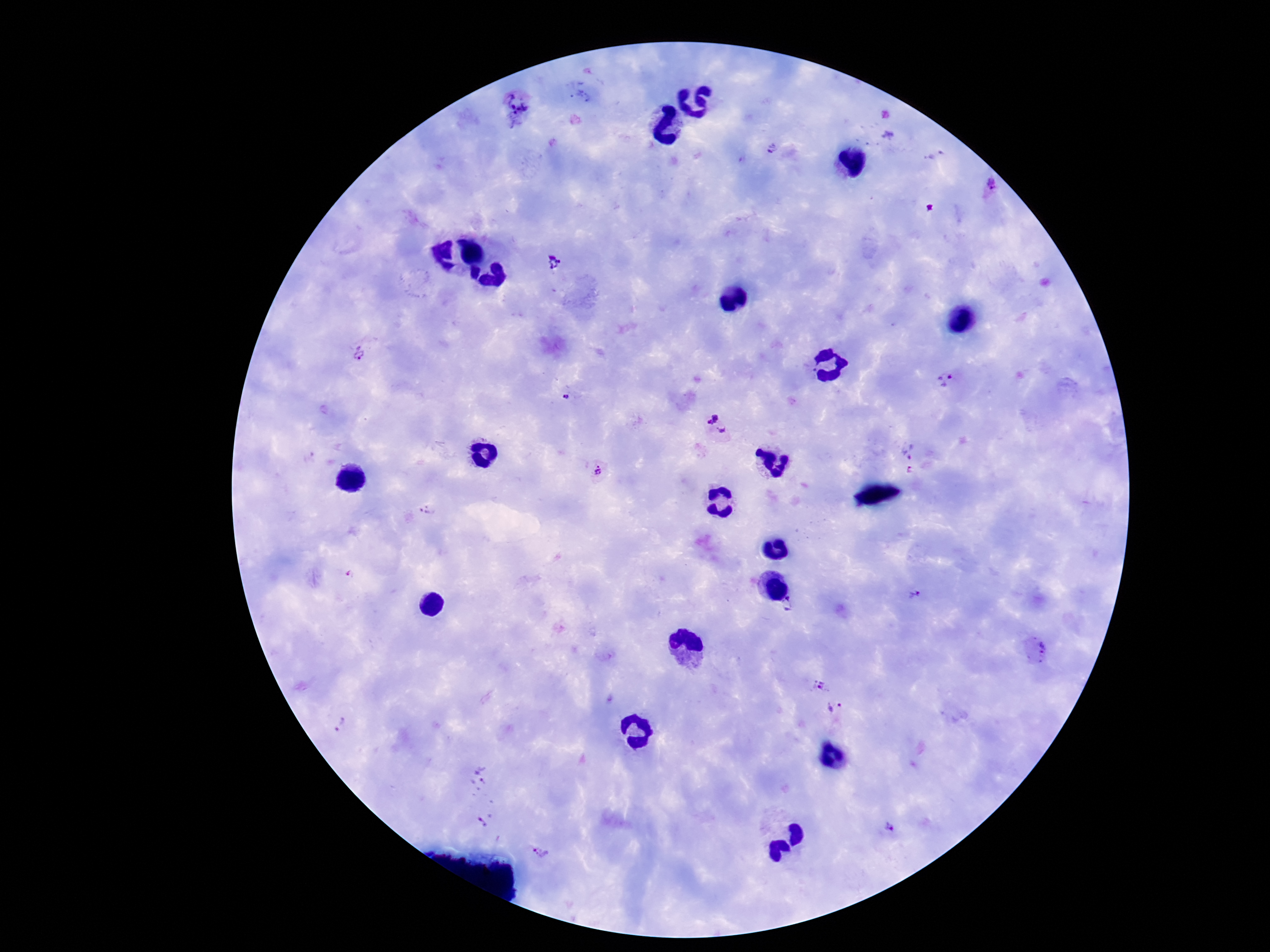
field of view = one from this slide
patient malaria status = infected
stain = Giemsa
image size = 1270×952 pixels
Plasmodium parasite locations = approximate object centers, in pixels from the top-left corner: (x=582, y=94), (x=518, y=107), (x=771, y=148), (x=989, y=190), (x=555, y=265), (x=360, y=352), (x=949, y=382), (x=566, y=398), (x=716, y=426), (x=910, y=451), (x=910, y=471), (x=598, y=472), (x=426, y=511), (x=916, y=594), (x=789, y=606), (x=1034, y=651), (x=819, y=685), (x=836, y=711), (x=341, y=723), (x=479, y=777), (x=487, y=818), (x=891, y=827), (x=541, y=853)
magnification = 100x
capture = smartphone camera through the microscope eyepiece
preparation = thick blood smear